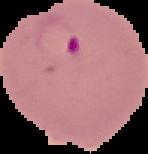

preparation = thin blood film
image size = 148×154 pixels
result = malaria parasites identified
image type = segmented cell region on a black background